State which parasite is depicted.
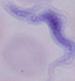

A trypanosome.

1000x magnification. Photomicrograph.